Outline each Plasmodium ovale-infected red blood cell.
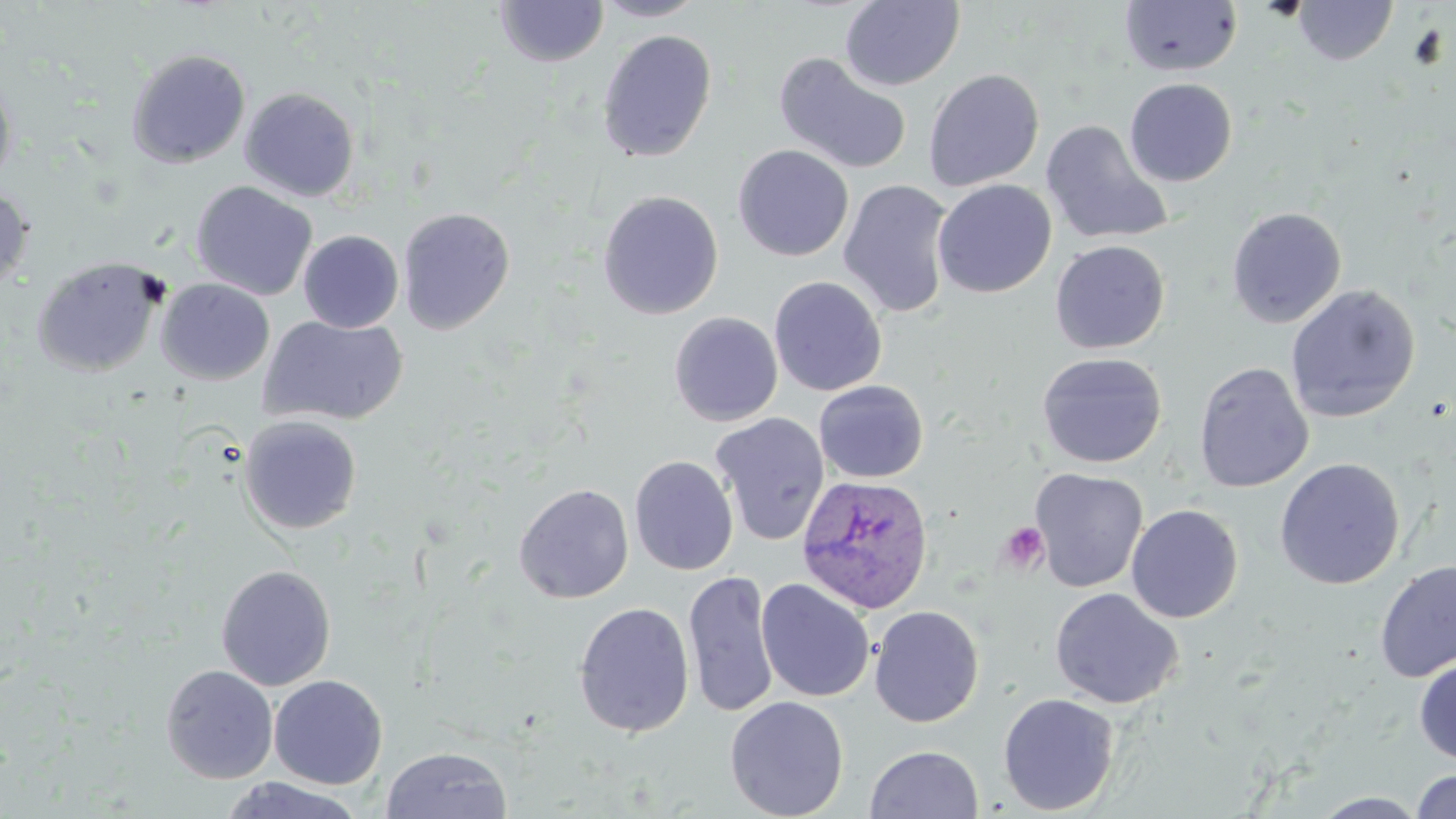

Approximate bounding boxes as [x1, y1, x2, y2] in pixels.
Plasmodium ovale-infected red blood cells: [796, 473, 934, 619].

Uninfected red blood cell locations: [591, 0, 709, 22], [839, 0, 965, 91], [493, 1, 609, 67], [1119, 1, 1242, 77], [1292, 1, 1398, 65], [597, 29, 718, 162], [126, 48, 251, 168], [773, 51, 913, 176], [923, 68, 1045, 192], [0, 70, 17, 193], [1124, 78, 1237, 186], [239, 87, 359, 202], [1040, 120, 1173, 246], [733, 144, 854, 262], [838, 179, 956, 318], [932, 179, 1057, 298], [191, 181, 318, 301], [0, 187, 32, 294], [597, 190, 724, 320], [1226, 206, 1347, 328], [397, 207, 516, 335], [298, 230, 404, 333], [1050, 239, 1170, 354], [32, 256, 165, 377], [769, 276, 887, 396], [156, 278, 275, 385], [1284, 284, 1421, 423], [669, 311, 783, 426], [259, 314, 409, 426], [1036, 352, 1167, 468], [1194, 361, 1314, 493], [813, 380, 929, 483], [710, 412, 830, 546], [238, 415, 362, 535], [629, 454, 739, 575], [1274, 457, 1406, 590], [1029, 468, 1148, 593], [514, 483, 634, 604], [1126, 504, 1243, 623], [1375, 560, 1455, 683], [215, 564, 336, 691], [683, 570, 779, 718], [755, 578, 875, 702], [1050, 588, 1184, 709], [573, 601, 695, 737], [869, 604, 984, 728], [1414, 659, 1456, 764], [160, 664, 279, 784], [269, 674, 388, 790], [997, 692, 1120, 815], [724, 695, 849, 819], [865, 744, 984, 819], [380, 746, 513, 819], [1411, 769, 1456, 819], [217, 777, 365, 819], [1311, 792, 1432, 818]. Platelet locations: [997, 521, 1050, 576]. Slide-level diagnosis: Plasmodium ovale. Image is 1456×819 pixels. Thin blood smear. May-Grünwald-Giemsa-stained preparation. Captured at 1000x magnification. Optical microscopy. One field of a larger specimen.